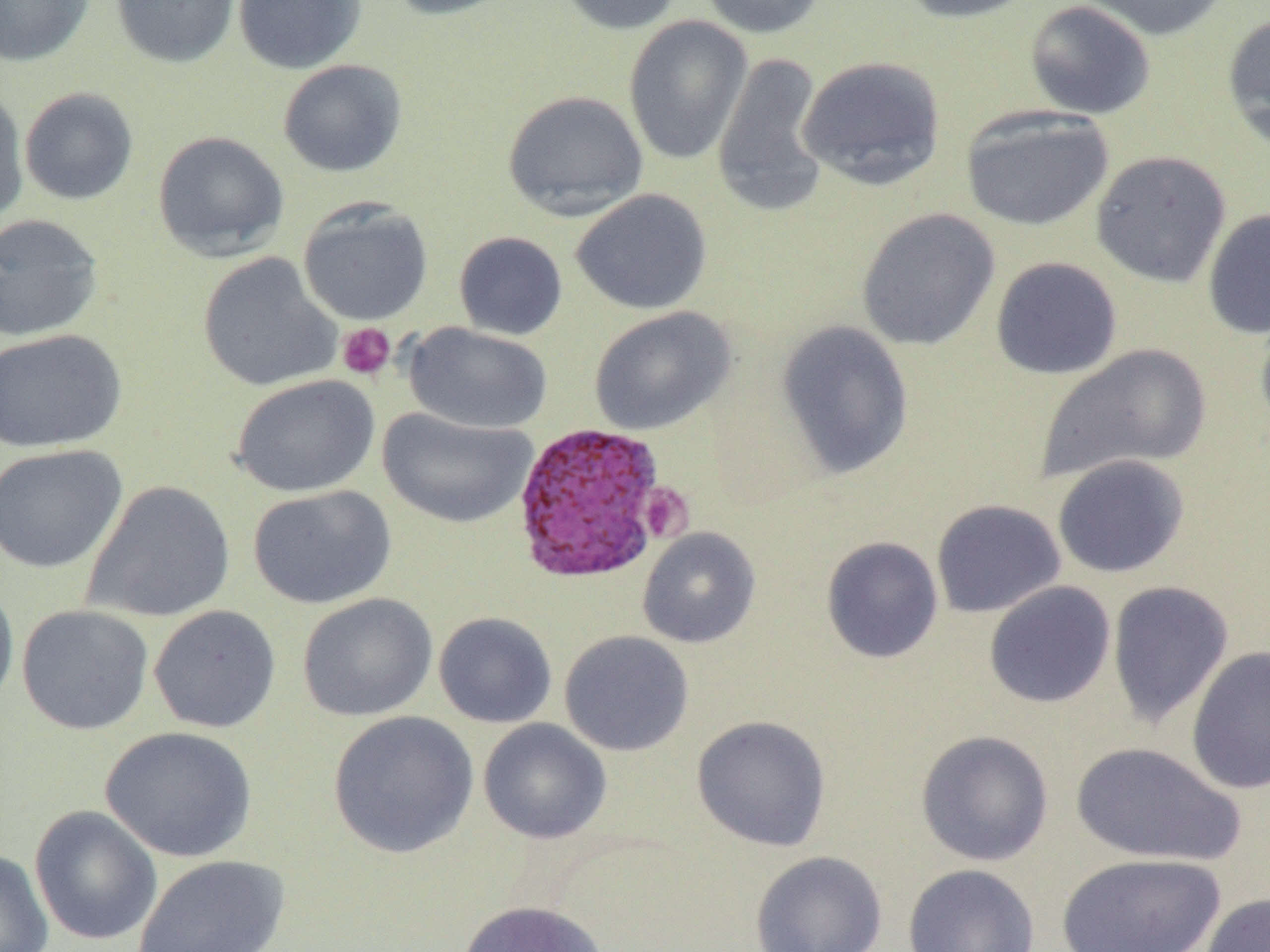

slide-level diagnosis = Plasmodium vivax
preparation = thin blood film
platelet locations = approximate bounding boxes as (x1,y1)-(x2,y2) corner pairs in pixels: (336,322)-(396,381), (638,482)-(694,543)
Plasmodium vivax-infected red blood cell locations = approximate bounding boxes as (x1,y1)-(x2,y2) corner pairs in pixels: (510,421)-(669,585)
magnification = 1000x
modality = light microscopy
field of view = one of a larger specimen
uninfected red blood cell locations = approximate bounding boxes as (x1,y1)-(x2,y2) corner pairs in pixels: (0,0)-(95,67), (110,0)-(240,68), (232,0)-(367,75), (383,0)-(517,21), (554,0)-(685,35), (697,0)-(827,39), (896,0)-(1041,24), (1075,0)-(1233,42), (1023,1)-(1157,120), (1221,11)-(1270,152), (622,16)-(754,166), (711,51)-(831,219), (797,54)-(946,191), (278,59)-(407,178), (0,85)-(29,225), (18,87)-(139,205), (502,89)-(648,221), (960,107)-(1114,232), (152,130)-(290,261), (1091,149)-(1231,288), (570,188)-(712,315), (297,199)-(434,327), (856,208)-(1000,351), (1202,208)-(1270,339), (0,214)-(105,342), (454,231)-(568,340), (197,252)-(342,392), (990,257)-(1123,380), (1255,304)-(1270,432), (588,305)-(736,436), (776,320)-(914,479), (404,322)-(553,434), (0,328)-(127,453), (1036,343)-(1212,483), (231,374)-(380,498), (378,408)-(538,529), (0,444)-(129,573), (1051,454)-(1190,579), (81,480)-(236,623), (248,484)-(396,610), (930,499)-(1066,619), (637,527)-(761,648), (821,535)-(943,664), (0,579)-(19,714), (1106,579)-(1235,729), (983,581)-(1116,709), (297,592)-(438,722), (16,604)-(154,735), (148,604)-(281,733), (433,612)-(557,728), (559,630)-(694,756), (1186,645)-(1270,795), (327,710)-(478,858), (691,715)-(832,851), (477,718)-(613,844), (100,726)-(257,863), (915,729)-(1054,866), (1071,740)-(1247,868), (29,805)-(163,945), (0,849)-(54,952), (750,850)-(888,952), (1054,852)-(1226,952), (132,854)-(290,952), (902,863)-(1040,952), (1199,892)-(1270,952), (457,900)-(609,952)
image size = 1270×952 pixels